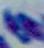

magnification = 1000x
identification = Toxoplasma gondii
modality = micrograph